Assess the background quality.
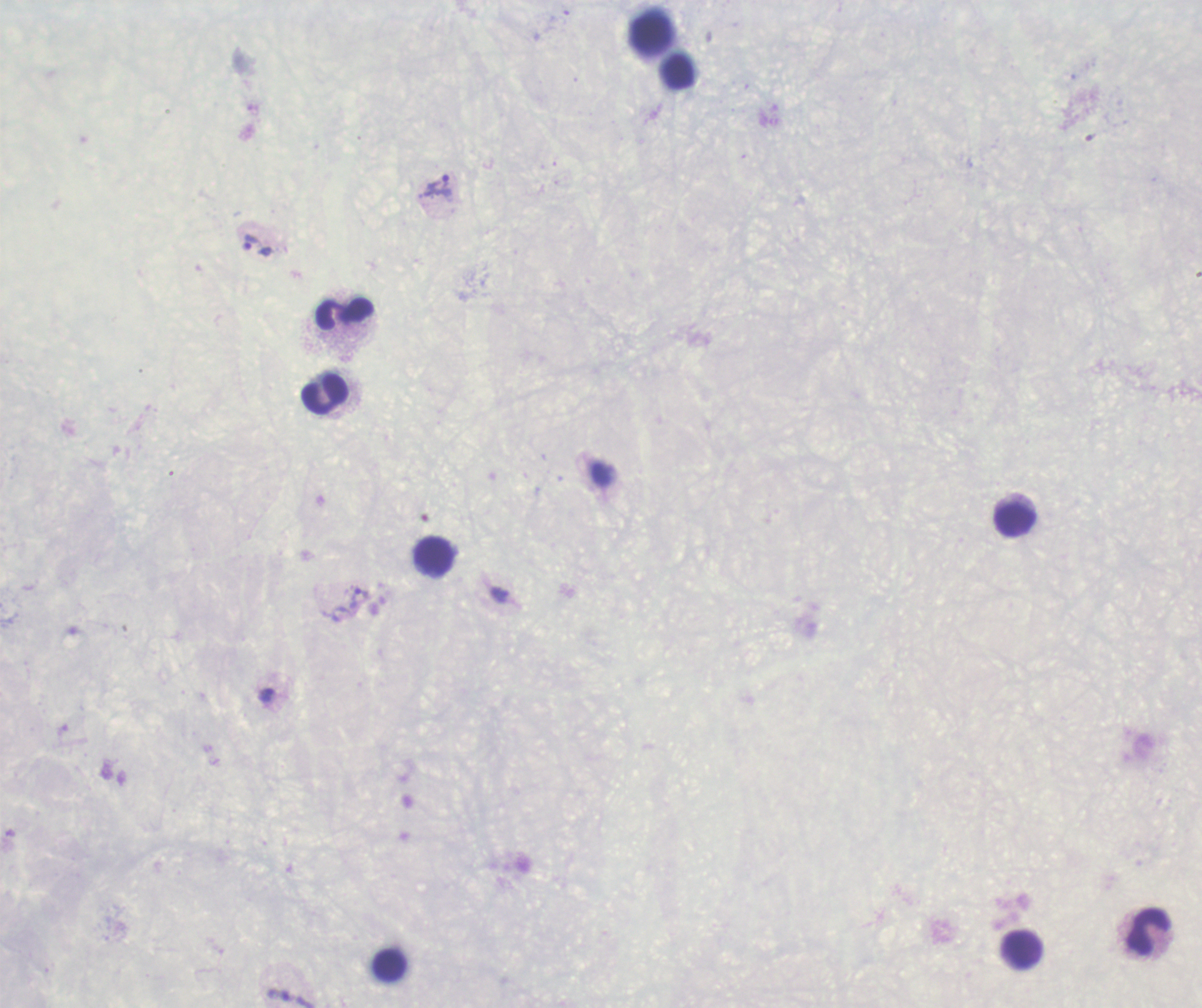
Poor.

Approximate object centers, in pixels from the top-left corner. Leukocyte locations: (x=651, y=34), (x=678, y=71), (x=345, y=315), (x=325, y=394), (x=1016, y=520), (x=434, y=556), (x=1149, y=930), (x=1023, y=950), (x=390, y=965). Trophozoite locations: (x=438, y=187), (x=258, y=245), (x=360, y=597), (x=267, y=696). Romanowsky stain. Previously used in a real diagnosis. Image is 1202×1008 pixels. Result: malaria parasites identified. Thick blood film. One field from this slide. Captured at 100x magnification. Coloration quality: bad.